Classify this cell by malaria status.
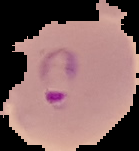
Parasitized.

{
  "preparation": "thin blood smear",
  "image_size": "139×151 pixels",
  "image_type": "cell region segmented out of the field of view; surrounding area masked to black"
}